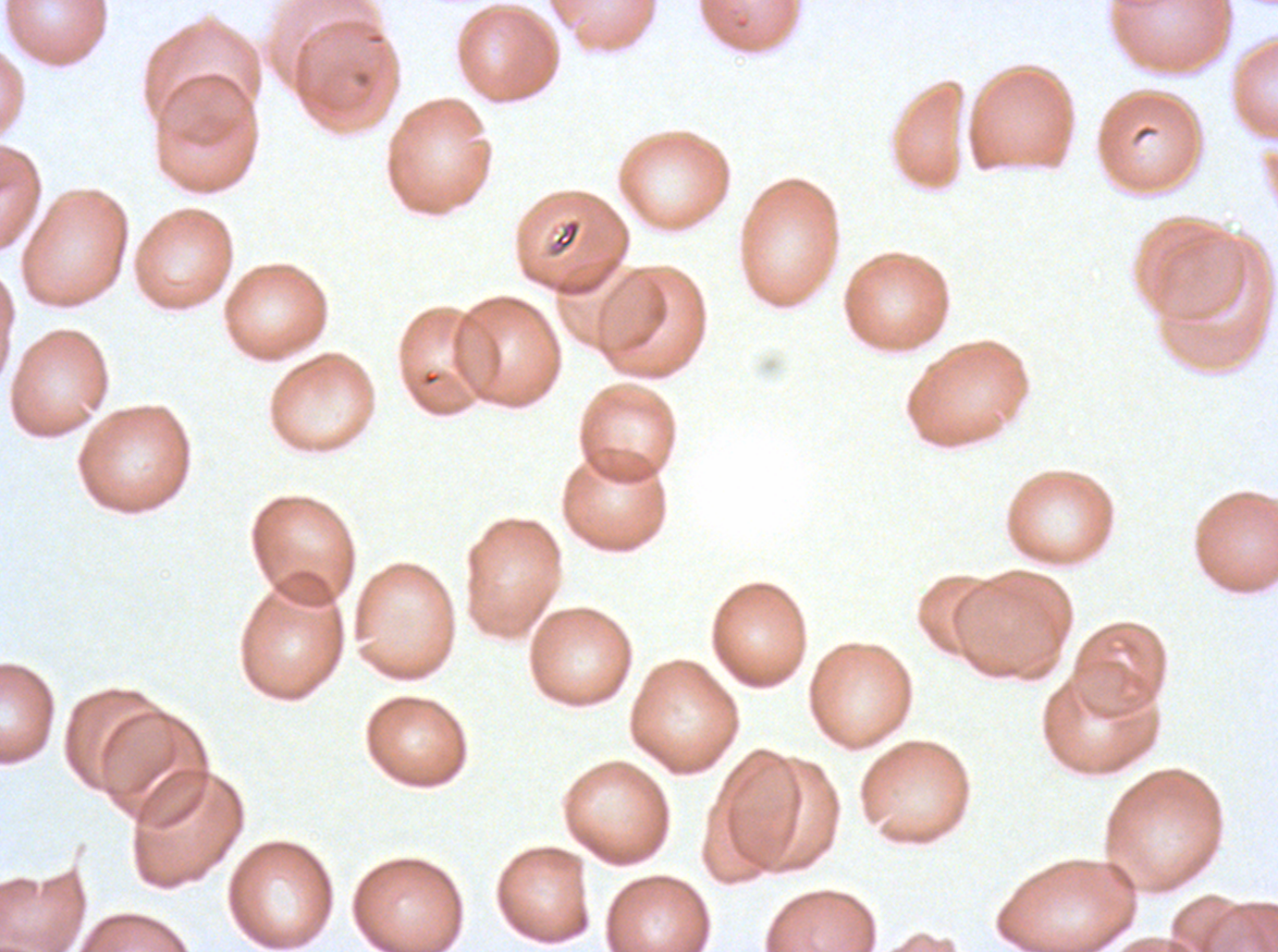
Approximate bounding rectangles given as corner coordinates in pixels from the top-left. Debris locations: (x1=351, y1=67, x2=373, y2=90), (x1=547, y1=217, x2=582, y2=258). Giemsa stain. Image is 1278×952 pixels. Thin blood smear. Plasmodium falciparum cultured ex vivo for 24 to 48 hours, from a patient in The Gambia. One sub-image of a larger composite.